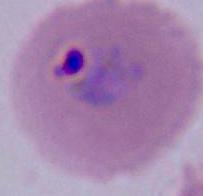

identification = Plasmodium
magnification = 400x or 1000x
modality = micrograph